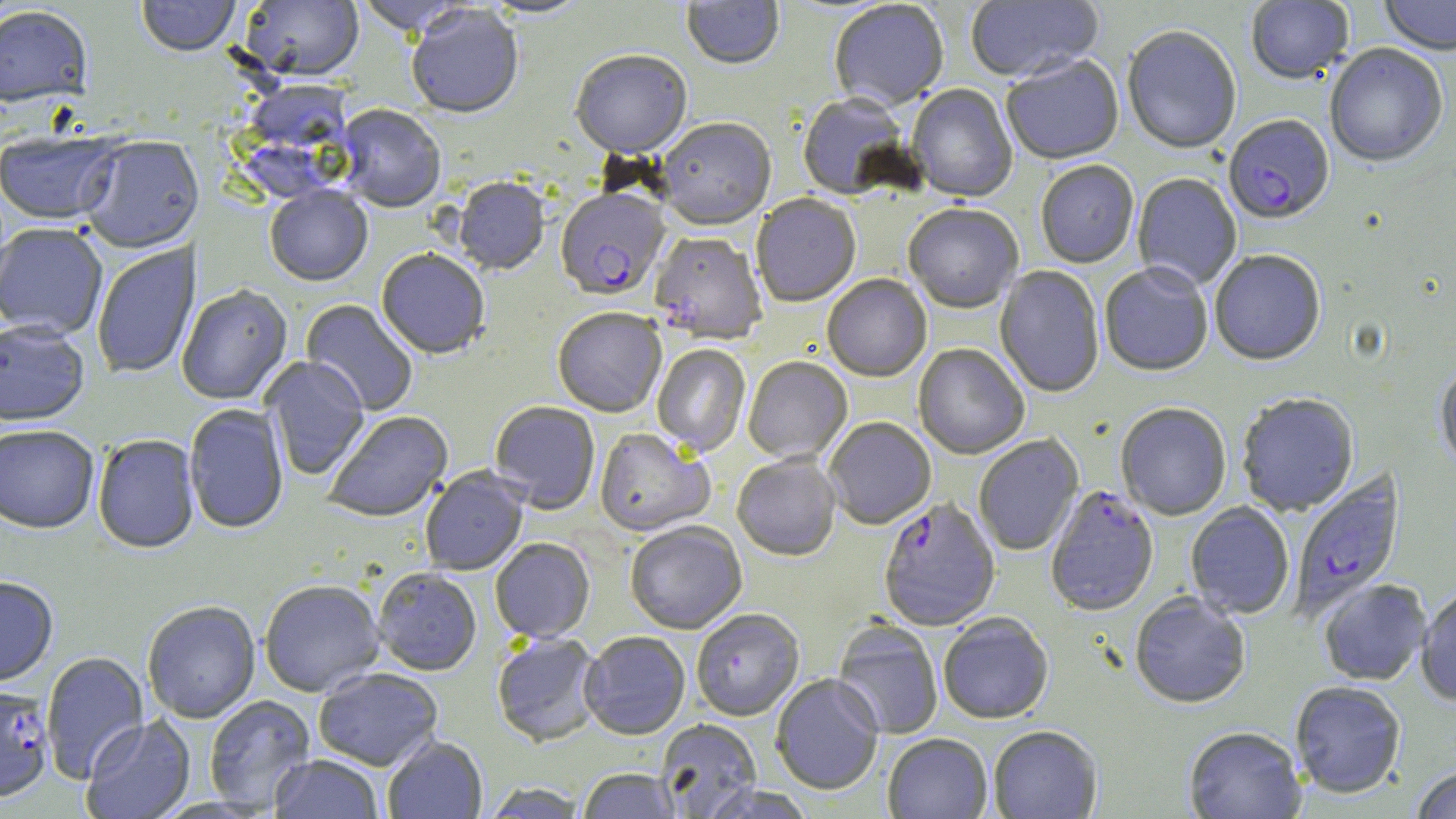

Approximate bounding boxes as (x1, y1, x2, y2) in pixels. Uninfected red blood cell locations: (136, 0, 240, 59), (354, 0, 476, 38), (480, 0, 591, 20), (682, 0, 784, 72), (966, 0, 1104, 85), (1379, 0, 1456, 58), (239, 1, 364, 83), (1246, 1, 1354, 86), (829, 2, 949, 112), (0, 6, 94, 109), (407, 6, 524, 122), (1121, 27, 1241, 156), (1325, 45, 1448, 170), (570, 51, 692, 161), (1001, 56, 1124, 167), (907, 85, 1018, 204), (797, 94, 912, 202), (335, 106, 446, 215), (656, 120, 776, 233), (0, 131, 123, 226), (80, 138, 203, 255), (1036, 162, 1139, 270), (1133, 174, 1242, 291), (453, 179, 549, 276), (264, 187, 373, 288), (751, 195, 861, 309), (903, 205, 1022, 315), (0, 225, 108, 341), (649, 234, 767, 346), (92, 241, 201, 380), (376, 251, 490, 360), (1210, 252, 1326, 368), (1099, 264, 1213, 378), (995, 266, 1105, 398), (822, 275, 932, 383), (176, 285, 293, 406), (301, 299, 418, 416), (553, 310, 667, 419), (0, 322, 90, 429), (914, 344, 1029, 461), (652, 345, 750, 457), (261, 357, 370, 480), (743, 358, 853, 465), (1435, 364, 1456, 473), (1237, 395, 1359, 516), (489, 402, 600, 515), (184, 404, 289, 535), (1116, 404, 1231, 521), (323, 411, 453, 524), (824, 418, 936, 530), (0, 426, 99, 536), (594, 428, 714, 537), (974, 434, 1084, 556), (93, 435, 200, 555), (732, 455, 841, 561), (420, 468, 529, 576), (1186, 502, 1295, 620), (626, 523, 747, 635), (490, 539, 595, 644), (373, 569, 482, 677), (0, 577, 58, 689), (1318, 580, 1431, 686), (260, 581, 385, 698), (1416, 587, 1456, 706), (1130, 594, 1250, 709), (143, 597, 384, 712), (142, 602, 260, 724), (691, 610, 804, 722), (939, 615, 1053, 725), (832, 621, 943, 739), (580, 633, 690, 742), (492, 634, 604, 748), (40, 651, 150, 783), (315, 668, 443, 772), (771, 675, 884, 795), (1290, 682, 1406, 799), (204, 695, 315, 813), (81, 716, 196, 819), (656, 720, 762, 817), (988, 727, 1102, 819), (1184, 728, 1307, 819), (882, 734, 992, 819), (383, 737, 487, 819), (268, 756, 383, 819), (1410, 766, 1456, 819), (577, 769, 682, 818), (481, 783, 588, 818), (698, 785, 817, 819). Plasmodium falciparum-infected red blood cell locations: (1223, 116, 1335, 226), (556, 191, 670, 303), (1289, 471, 1405, 624), (1044, 486, 1158, 618), (879, 500, 1000, 633), (0, 686, 54, 803). Slide-level diagnosis: Plasmodium falciparum. One field of a larger specimen. Thin blood film. Optical microscopy. 1000x magnification. May-Grünwald-Giemsa stain. Image is 1456×819 pixels.